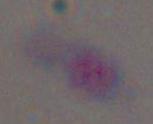

Summary:
  - Identification: Toxoplasma gondii
  - Magnification: 1000x
  - Modality: photomicrograph